Name the cell type shown.
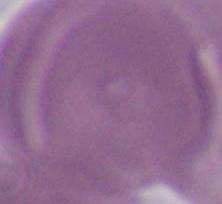

An erythrocyte.

{
  "magnification": "1000x",
  "modality": "photomicrograph"
}